State which parasite is depicted.
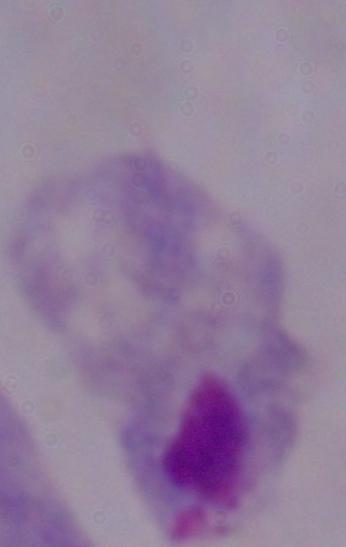

A trichomonad.

Micrograph. 1000x magnification.